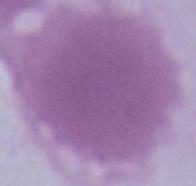

A red blood cell is seen. 1000x magnification. Photomicrograph.